Comment on the morphology of the erythrocytes.
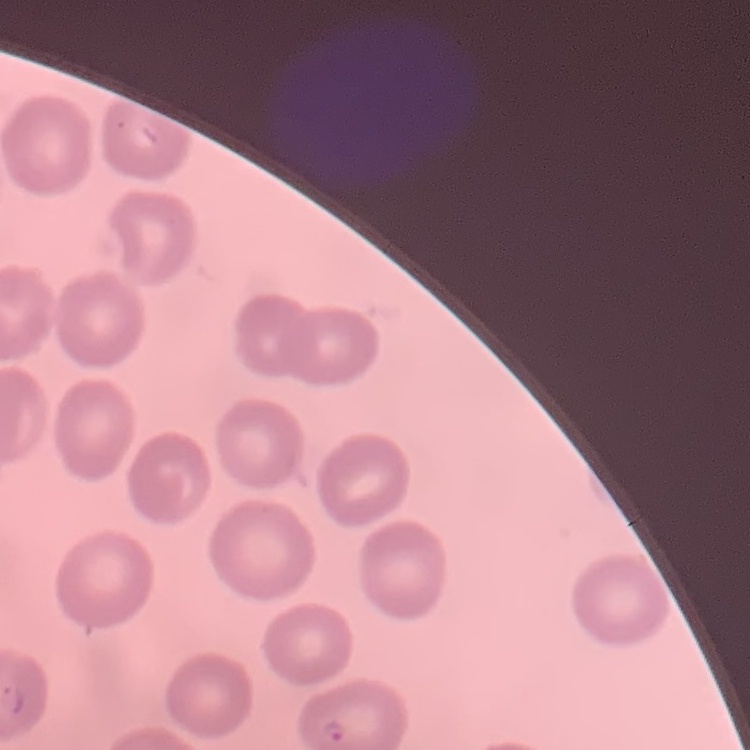
No rouleaux formation.

Summary:
  - Preparation: thin blood film
  - Stain: Field's or Giemsa
  - Image type: one tile cut from a larger photomicrograph